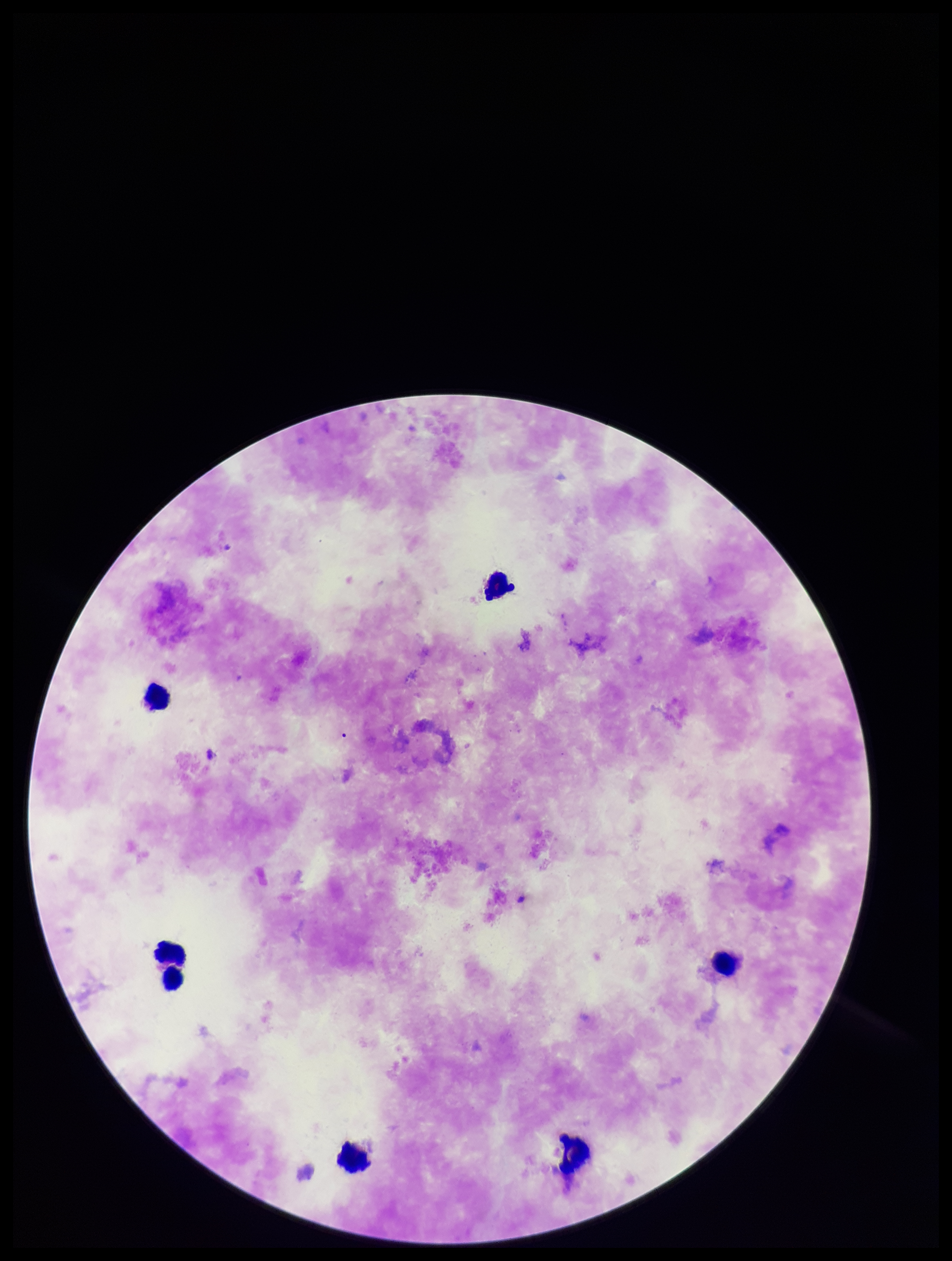

Summary:
  - Capture: smartphone photograph through the microscope eyepiece
  - Stain: Giemsa
  - Plasmodium parasites: none identified
  - Patient malaria status: negative
  - Parasite count: 0
  - Field of view: one from this slide
  - Leukocyte count: 7
  - Image size: 952×1261 pixels
  - Preparation: thick smear